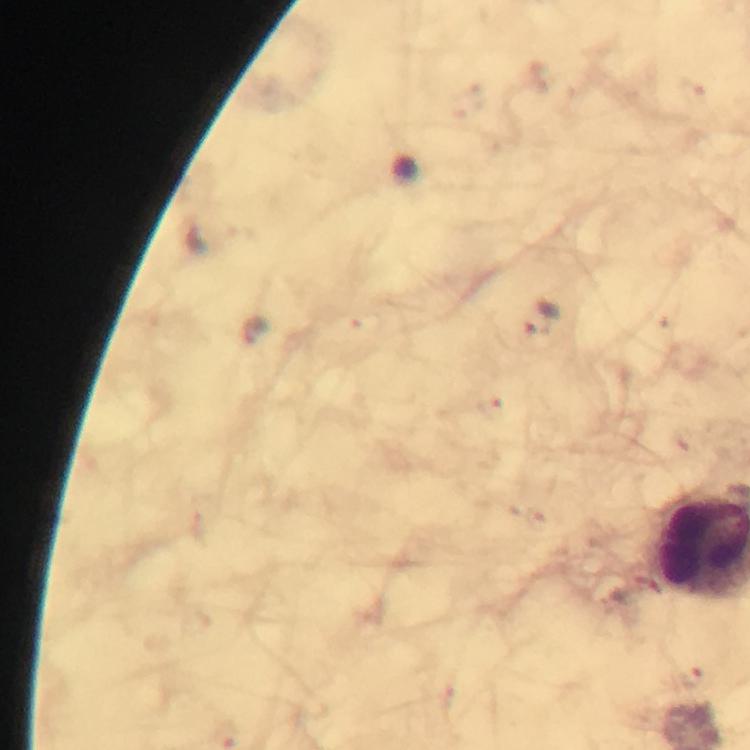
Approximate centers as {x, y} in pixels. Malaria parasite locations: {543, 322}, {692, 679}. At 100x magnification. Thick smear. From a diagnostic examination for malaria. Smartphone photograph taken through a microscope. A crop from one field of view. Immersion oil was used. Giemsa-stained preparation. Image is 750×750 pixels.